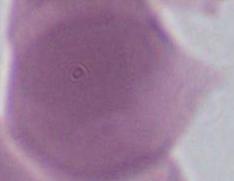

Summary:
  - Identification: Plasmodium
  - Modality: photomicrograph
  - Magnification: 400x or 1000x